Assess the morphology of the red blood cells.
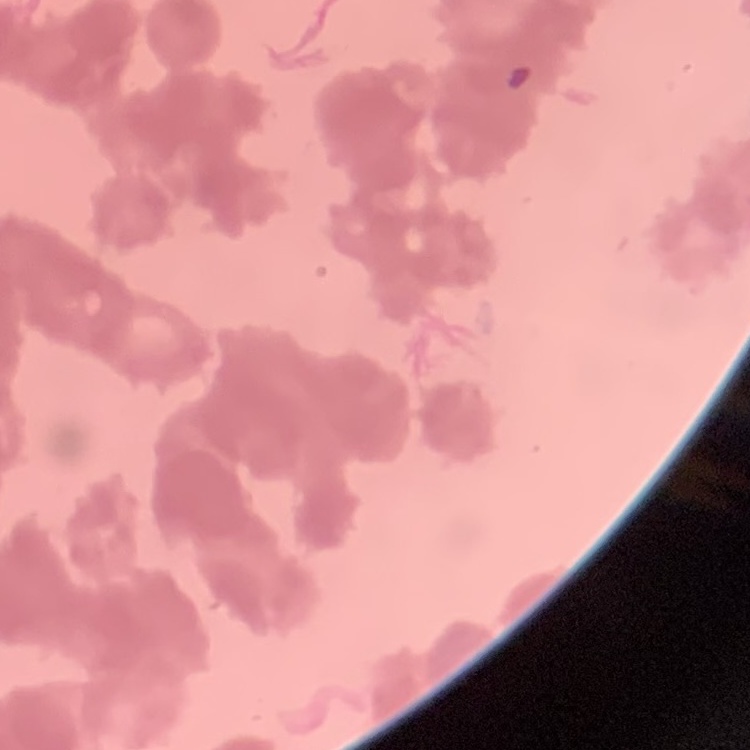

They show rouleaux formation.

Summary:
  - Stain: Field's or Giemsa
  - Image type: square crop of a larger photomicrograph
  - Preparation: thin peripheral smear